Point out each leukocyte.
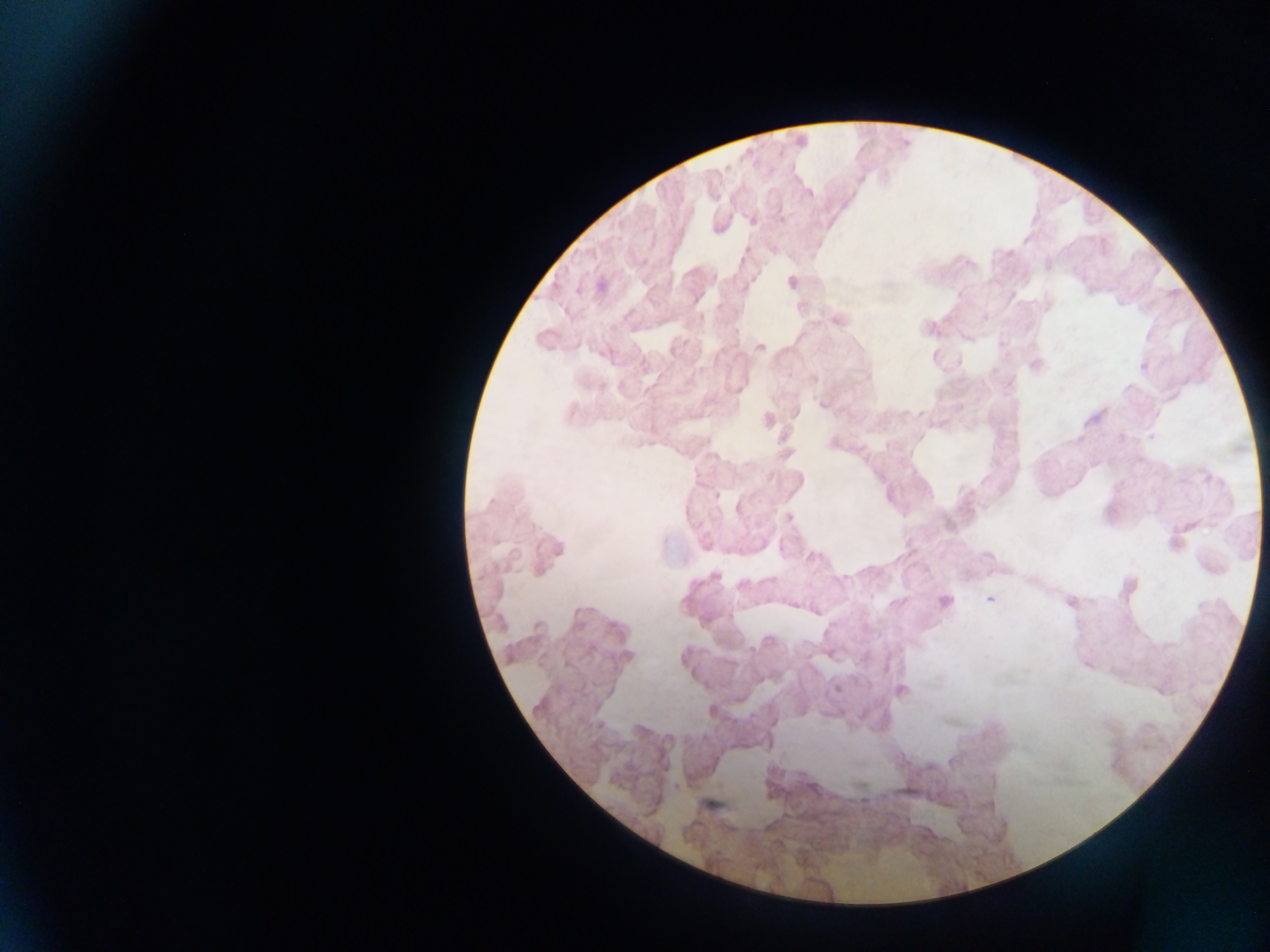
No leukocytes observed.

field_of_view: single
country: Ghana
image_size: 1270×952 pixels
preparation: thick blood smear
malaria_parasite_locations: 'approximate centers as (x, y) in pixels: (808, 193), (718, 227), (1048, 265), (790, 281), (601, 285), (837, 319), (965, 337), (1003, 344), (759, 346), (1035, 365), (813, 377), (738, 390), (822, 404), (795, 412), (767, 420), (785, 453), (717, 496), (738, 507), (788, 518), (1176, 542), (989, 598), (944, 601), (1070, 601), (900, 690), (708, 804)'
capture: mobile-phone photograph through a microscope